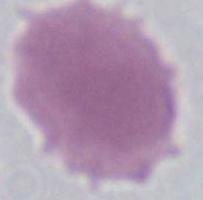

modality = micrograph
magnification = 1000x
identification = red blood cell